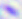

Photomicrograph. Toxoplasma gondii is shown. Captured at 400x magnification.